Locate every Trypanosoma brucei.
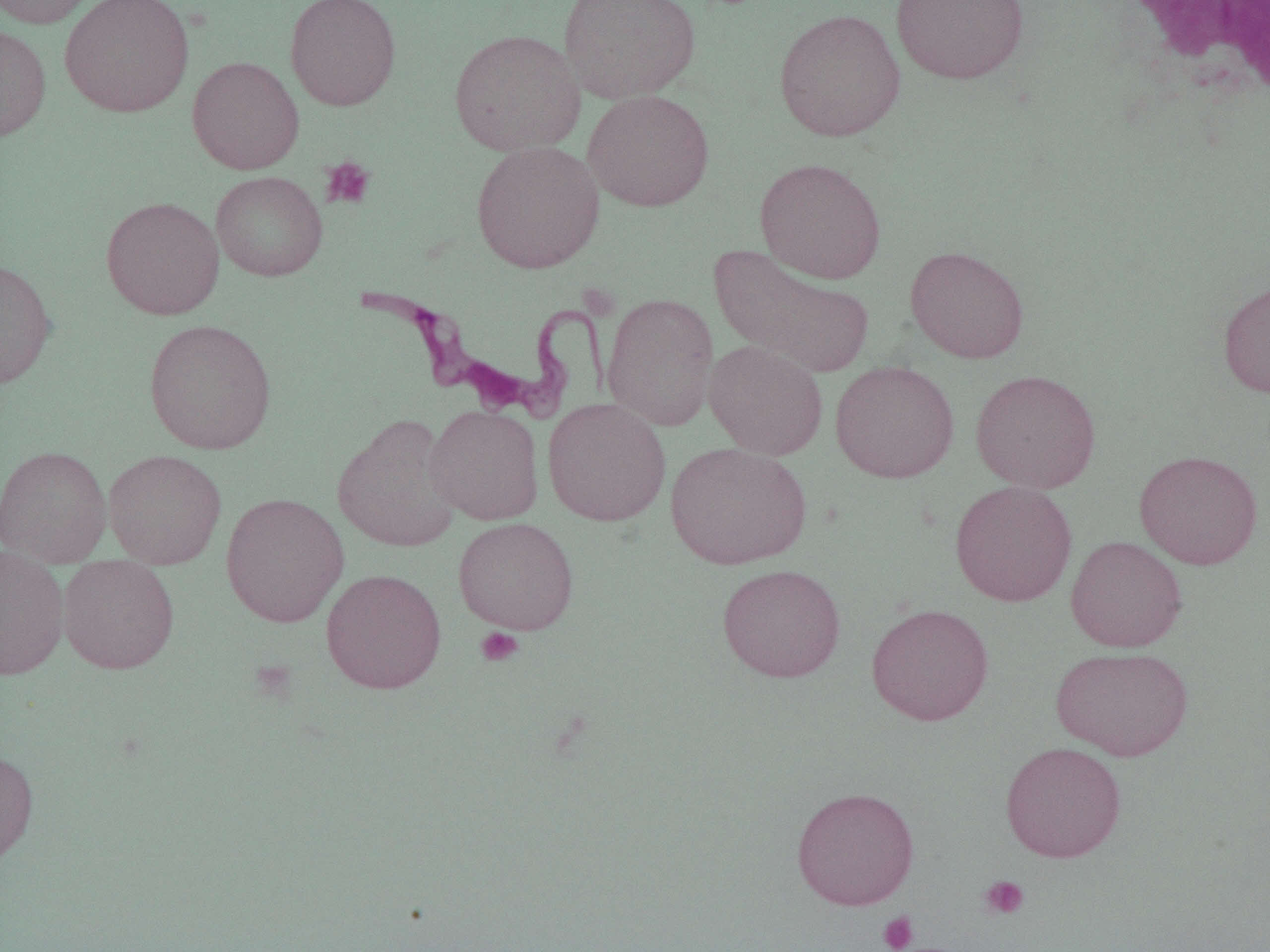
Approximate bounding boxes as (x1,y1)-(x2,y2) corner pairs in pixels.
Trypanosoma brucei: (355,287)-(615,424).

Uninfected red blood cell locations: (0,0)-(102,29), (59,0)-(194,118), (284,0)-(401,111), (558,0)-(702,104), (890,0)-(1030,85), (773,8)-(906,142), (0,23)-(51,142), (449,29)-(585,156), (187,55)-(304,175), (583,90)-(715,212), (470,141)-(605,274), (755,157)-(887,284), (210,171)-(328,282), (101,196)-(225,320), (708,244)-(874,379), (905,245)-(1029,363), (0,257)-(57,389), (1217,278)-(1270,398), (602,292)-(719,432), (143,318)-(277,454), (704,340)-(828,460), (830,360)-(959,483), (970,369)-(1102,494), (542,398)-(671,526), (424,405)-(544,525), (332,415)-(462,553), (666,441)-(812,570), (0,445)-(112,566), (103,449)-(227,570), (1134,449)-(1263,569), (950,480)-(1077,606), (220,492)-(349,627), (453,517)-(579,635), (1065,536)-(1187,652), (0,546)-(70,680), (58,556)-(179,673), (717,564)-(846,682), (321,568)-(447,694), (866,603)-(994,726), (1050,646)-(1194,760), (1001,742)-(1126,862), (0,747)-(39,872), (791,786)-(920,910). Platelet locations: (321,156)-(376,210), (475,627)-(524,667), (979,875)-(1030,920), (878,911)-(918,952). White blood cell locations: (1109,2)-(1270,114). Slide-level diagnosis: Trypanosoma brucei. Single field of view. Image is 1270×952 pixels. Thin blood film. Captured at 1000x magnification. Light microscopy.